Assess this cell for malaria.
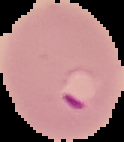

It is parasitized.

preparation = thin blood smear
image size = 124×142 pixels
image type = segmented cell region with the area outside set to black